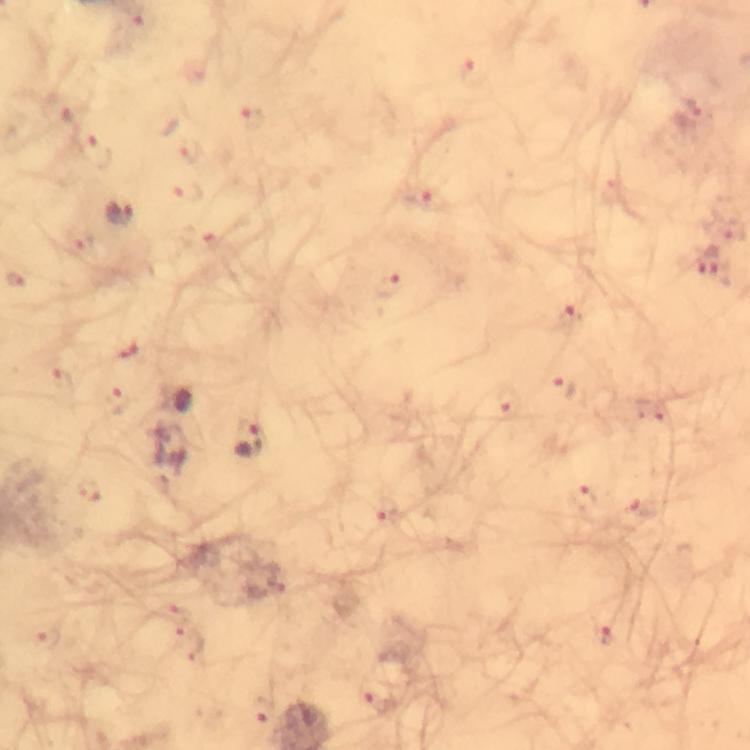
Approximate object centers, in pixels from the top-left corner.
Summary:
  - Malaria parasite locations: (x=691, y=108), (x=419, y=196), (x=119, y=213), (x=709, y=262), (x=388, y=287), (x=569, y=316), (x=564, y=386), (x=507, y=401), (x=247, y=438), (x=582, y=496), (x=385, y=508), (x=606, y=633), (x=376, y=700), (x=262, y=709)
  - Image size: 750×750 pixels
  - Cropped from: a single field of view
  - Magnification: 100x
  - Preparation: thick blood smear
  - Capture: smartphone camera through the microscope
  - Stain: Giemsa
  - Immersion oil: used
  - Context: from a malaria diagnostic workup